State which parasite is depicted.
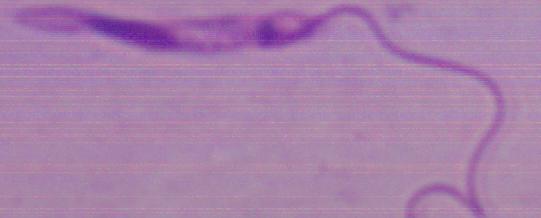
This is Leishmania.

Summary:
  - Magnification: 1000x
  - Modality: photomicrograph